Classify this cell by malaria status.
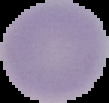
Uninfected.

image size = 109×103 pixels
preparation = thin blood film
image type = segmented cell region with the area outside set to black